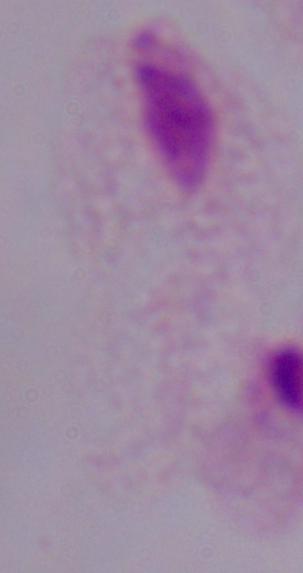
Captured at 1000x magnification. A trichomonad is seen. Micrograph.